Classify this cell by malaria status.
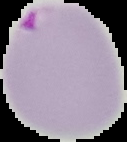
It is parasitized.

Segmented cell region on a black background. Image is 127×142 pixels. From a thin blood film.